Assess this cell for malaria.
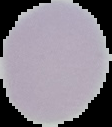

Uninfected.

preparation = thin blood film
image type = segmented cell region with the area outside set to black
image size = 112×127 pixels